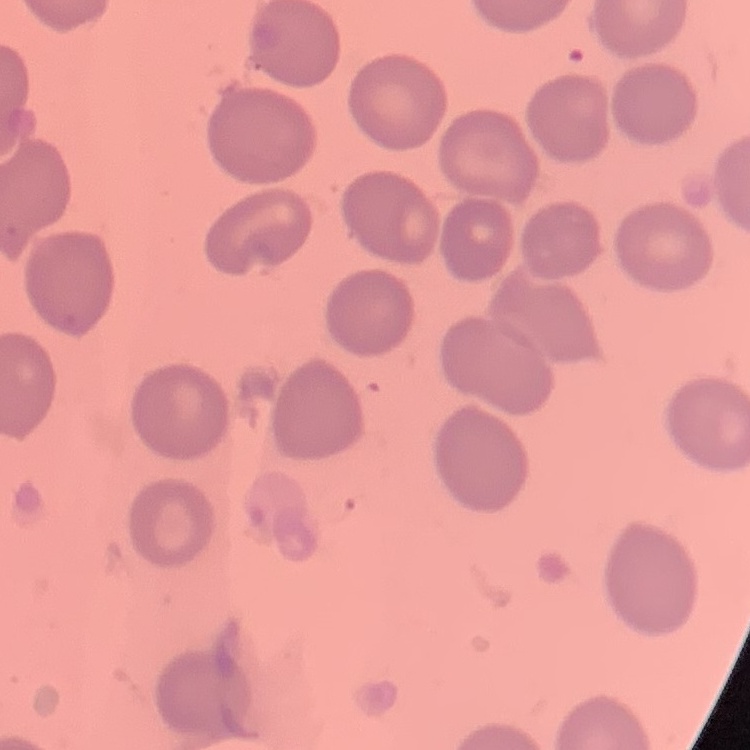 The erythrocytes exhibit no rouleaux formation. One tile cut from a larger photomicrograph. Thin peripheral smear. Field's or Giemsa stain.